Give the extent of all Plasmodium vivax-infected red blood cells.
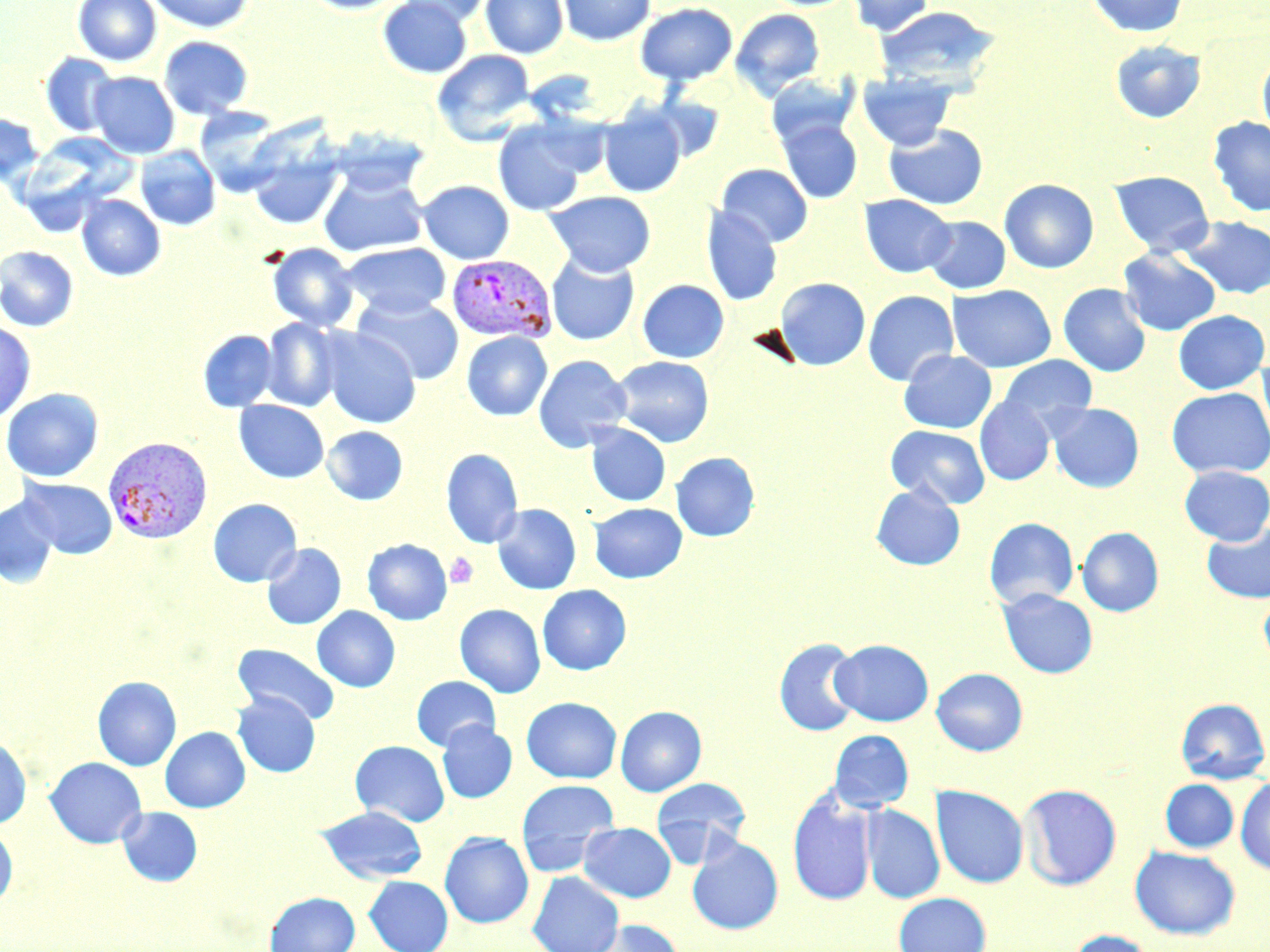
Approximate bounding boxes as [x1, y1, x2, y2] in pixels.
Plasmodium vivax-infected red blood cells: [447, 253, 557, 343], [103, 436, 213, 543].

Summary:
  - Platelet locations: [445, 552, 478, 588]
  - Uninfected red blood cell locations: [73, 0, 161, 66], [146, 0, 254, 34], [300, 0, 409, 14], [378, 0, 472, 78], [396, 0, 493, 27], [480, 0, 568, 59], [558, 0, 655, 46], [847, 0, 936, 36], [1085, 0, 1189, 38], [635, 2, 738, 86], [874, 6, 1001, 89], [730, 8, 825, 100], [159, 35, 253, 120], [1109, 40, 1207, 123], [432, 49, 536, 145], [40, 53, 119, 137], [1257, 53, 1270, 145], [89, 71, 180, 159], [857, 72, 957, 151], [766, 74, 859, 148], [195, 106, 288, 195], [599, 106, 687, 197], [0, 113, 44, 187], [1208, 116, 1270, 217], [777, 118, 862, 203], [492, 119, 591, 216], [883, 124, 988, 210], [328, 128, 430, 196], [16, 133, 134, 233], [135, 146, 221, 231], [248, 150, 343, 229], [717, 163, 813, 247], [318, 169, 429, 257], [1109, 170, 1214, 257], [999, 179, 1099, 273], [418, 180, 515, 264], [545, 190, 656, 277], [859, 194, 956, 278], [76, 195, 166, 281], [701, 205, 782, 306], [923, 215, 1011, 294], [1181, 216, 1270, 300], [340, 242, 451, 319], [266, 243, 359, 332], [0, 246, 79, 331], [1118, 248, 1221, 336], [546, 252, 640, 346], [774, 277, 870, 370], [637, 279, 729, 363], [1058, 283, 1151, 377], [947, 284, 1056, 373], [862, 290, 959, 386], [352, 294, 464, 384], [1173, 310, 1269, 394], [261, 318, 344, 411], [0, 320, 36, 424], [320, 327, 421, 428], [197, 330, 278, 412], [461, 331, 553, 421], [898, 350, 997, 434], [1257, 353, 1270, 447], [533, 354, 632, 452], [611, 355, 714, 447], [998, 355, 1098, 434], [1167, 387, 1270, 478], [1, 388, 103, 482], [974, 395, 1056, 485], [234, 400, 329, 483], [1047, 402, 1144, 493], [585, 423, 671, 506], [885, 425, 990, 509], [321, 426, 408, 505], [440, 448, 524, 548], [670, 451, 760, 541], [1179, 465, 1270, 545], [19, 477, 118, 558], [871, 484, 965, 571], [0, 496, 59, 588], [208, 498, 302, 587], [589, 502, 687, 583], [492, 503, 582, 595], [983, 517, 1079, 609], [1202, 522, 1270, 603], [1077, 527, 1164, 616], [362, 538, 452, 625], [261, 543, 346, 629], [537, 584, 631, 675], [998, 588, 1098, 678], [1258, 588, 1270, 670], [455, 604, 545, 698], [312, 606, 400, 692], [774, 637, 863, 736], [830, 639, 933, 726], [232, 643, 340, 725], [931, 667, 1028, 755], [92, 676, 181, 771], [411, 676, 501, 752], [232, 692, 321, 777], [521, 696, 621, 783], [1176, 697, 1270, 784], [615, 705, 707, 796], [437, 721, 517, 804], [160, 727, 250, 812], [829, 729, 914, 812], [0, 736, 31, 828], [349, 740, 450, 826], [44, 757, 146, 848], [1235, 776, 1270, 875], [651, 777, 751, 866], [515, 779, 620, 876], [1160, 779, 1238, 852], [1018, 783, 1122, 890], [931, 785, 1028, 888], [787, 790, 877, 906], [860, 804, 945, 904], [316, 805, 428, 883], [117, 806, 202, 886], [579, 822, 676, 902], [0, 825, 18, 908], [439, 831, 534, 928], [686, 835, 784, 935], [1130, 846, 1240, 939], [527, 871, 624, 952], [364, 875, 453, 952], [265, 891, 360, 952], [893, 892, 991, 952], [586, 919, 685, 952], [1065, 929, 1158, 952]
  - Slide-level diagnosis: Plasmodium vivax
  - Magnification: 1000x
  - Image size: 1270×952 pixels
  - Field of view: one of a larger specimen
  - Preparation: thin blood smear
  - Stain: May-Grünwald-Giemsa
  - Modality: optical microscopy